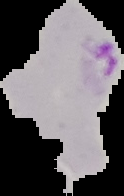

Segmented cell region on a black background. From a thin blood smear. Image is 124×196 pixels. Result: malaria parasites detected.